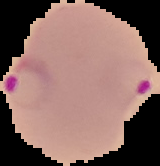
preparation = thin blood film
result = malaria parasites detected
image type = cell region segmented out of the field of view; surrounding area masked to black
image size = 160×166 pixels